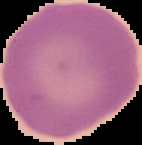

result = no Plasmodium parasites detected
preparation = thin blood film
image size = 142×145 pixels
image type = segmented cell region with the area outside set to black